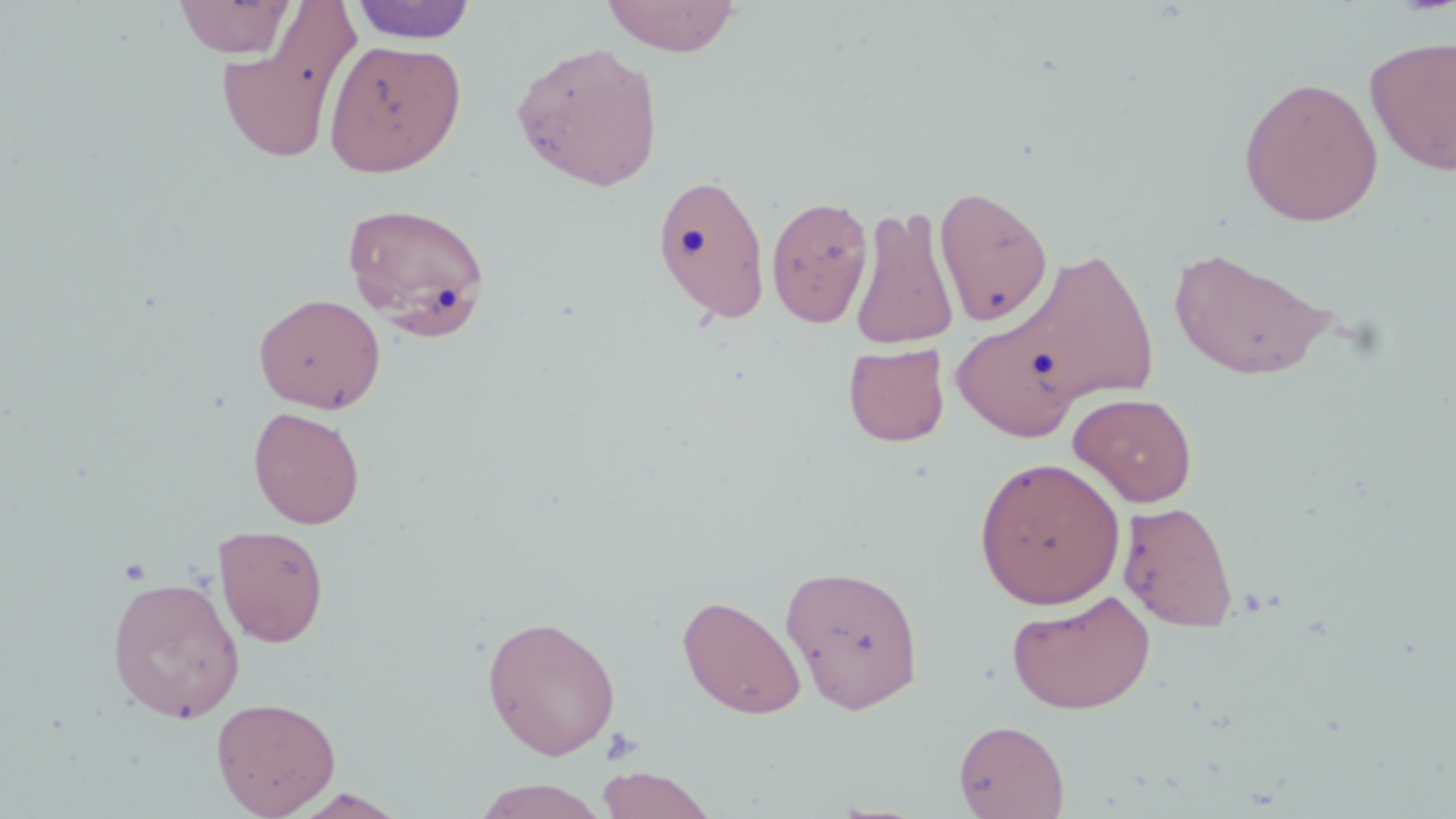

{
  "slide_level_diagnosis": "negative for blood parasites",
  "stain": "May-Grünwald-Giemsa",
  "modality": "light microscopy",
  "uninfected_red_blood_cell_locations": "approximate bounding boxes as named x1/y1/x2/y2 corners in pixels: (x1=173, y1=0, x2=297, y2=58), (x1=600, y1=0, x2=741, y2=56), (x1=349, y1=1, x2=477, y2=45), (x1=216, y1=9, x2=360, y2=165), (x1=1365, y1=34, x2=1456, y2=175), (x1=323, y1=39, x2=466, y2=177), (x1=510, y1=40, x2=664, y2=191), (x1=1238, y1=76, x2=1384, y2=226), (x1=651, y1=172, x2=771, y2=325), (x1=933, y1=184, x2=1054, y2=327), (x1=766, y1=195, x2=874, y2=327), (x1=341, y1=200, x2=492, y2=338), (x1=848, y1=204, x2=961, y2=350), (x1=1169, y1=243, x2=1338, y2=381), (x1=1013, y1=246, x2=1161, y2=408), (x1=254, y1=293, x2=386, y2=413), (x1=951, y1=317, x2=1082, y2=442), (x1=843, y1=343, x2=950, y2=446), (x1=1068, y1=392, x2=1198, y2=507), (x1=248, y1=407, x2=365, y2=529), (x1=974, y1=456, x2=1126, y2=609), (x1=1117, y1=501, x2=1238, y2=633), (x1=212, y1=524, x2=329, y2=648), (x1=780, y1=563, x2=925, y2=715), (x1=106, y1=575, x2=245, y2=722), (x1=1006, y1=589, x2=1156, y2=714), (x1=677, y1=594, x2=807, y2=720), (x1=481, y1=614, x2=621, y2=761), (x1=210, y1=696, x2=341, y2=818), (x1=953, y1=719, x2=1069, y2=818), (x1=595, y1=767, x2=718, y2=818), (x1=472, y1=779, x2=610, y2=817), (x1=287, y1=789, x2=410, y2=818)",
  "platelet_locations": "approximate bounding boxes as named x1/y1/x2/y2 corners in pixels: (x1=599, y1=726, x2=643, y2=766)",
  "image_size": "1456×819 pixels",
  "field_of_view": "one of a larger specimen",
  "magnification": "1000x",
  "preparation": "thin blood film"
}